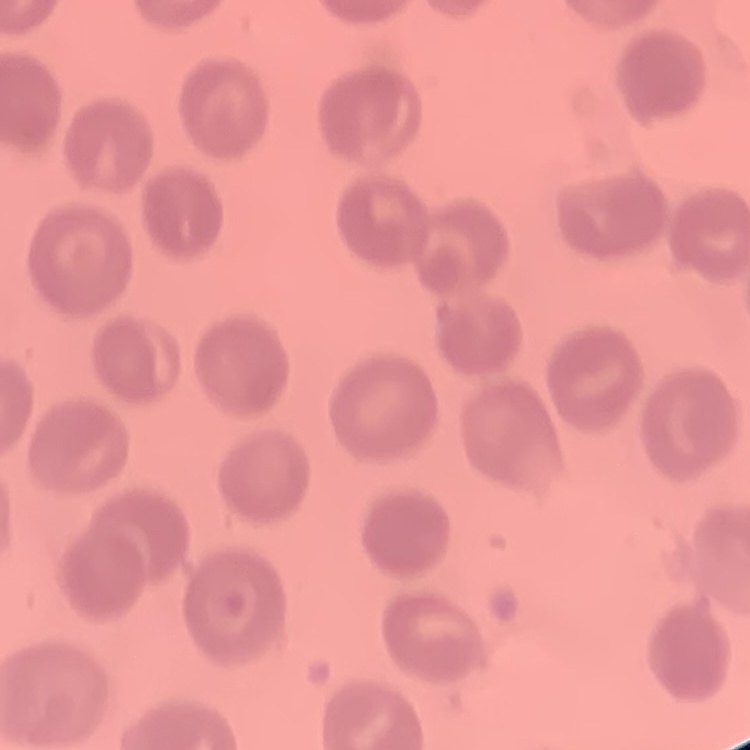

Summary:
  - Red blood cell morphology: no rouleaux formation
  - Image type: one tile cut from a larger photomicrograph
  - Stain: Field's or Giemsa
  - Preparation: thin blood film